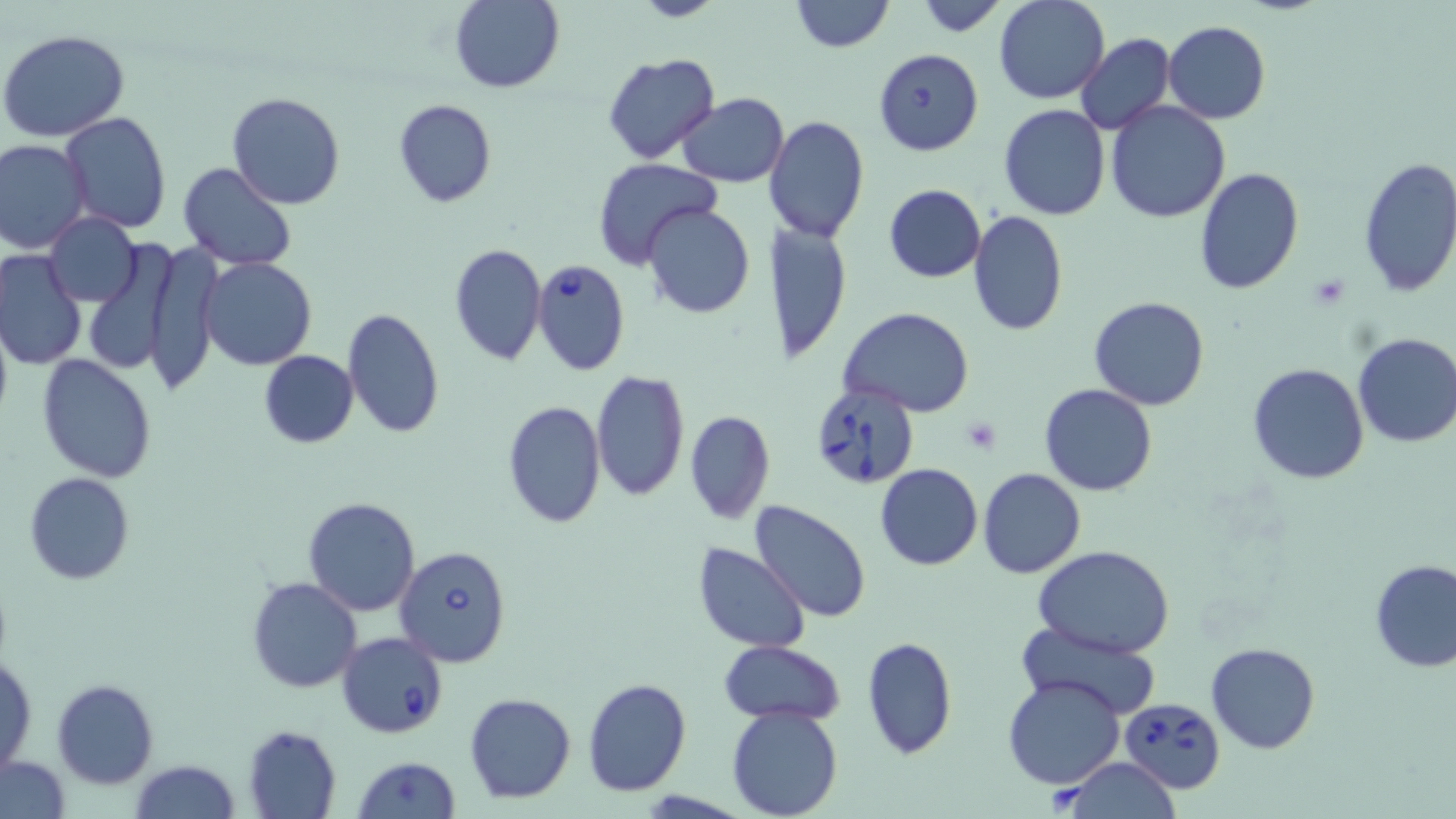
Approximate bounding boxes as (x1, y1, x2, y2) in pixels. Platelet locations: (959, 415, 1003, 453). Babesia divergens-infected red blood cell locations: (873, 48, 982, 157), (530, 258, 631, 376), (809, 380, 920, 489), (394, 543, 513, 667), (338, 632, 449, 738), (1119, 697, 1225, 795). Uninfected red blood cell locations: (449, 0, 565, 93), (790, 0, 892, 51), (913, 0, 1011, 36), (993, 0, 1109, 104), (1163, 20, 1271, 123), (1, 30, 130, 142), (1075, 34, 1174, 136), (604, 52, 719, 162), (227, 91, 345, 209), (676, 93, 789, 188), (393, 98, 496, 207), (1105, 100, 1232, 223), (999, 104, 1109, 220), (60, 111, 171, 231), (763, 115, 870, 244), (0, 139, 92, 255), (1356, 155, 1456, 298), (592, 158, 722, 272), (178, 163, 299, 271), (1193, 168, 1304, 295), (882, 184, 985, 283), (643, 203, 755, 318), (967, 210, 1069, 336), (45, 211, 142, 307), (767, 220, 851, 366), (83, 238, 181, 377), (146, 240, 223, 398), (448, 243, 546, 366), (0, 250, 87, 371), (200, 257, 316, 370), (1088, 295, 1210, 411), (341, 307, 442, 440), (839, 308, 974, 416), (0, 312, 12, 429), (1352, 331, 1456, 448), (257, 350, 360, 449), (36, 353, 158, 482), (1246, 363, 1370, 485), (590, 369, 691, 505), (1041, 383, 1157, 495), (502, 400, 605, 531), (684, 410, 774, 525), (874, 463, 984, 571), (977, 468, 1087, 580), (23, 472, 135, 584), (302, 496, 421, 617), (750, 500, 871, 622), (693, 543, 811, 653), (1035, 546, 1175, 657), (1369, 559, 1456, 672), (246, 576, 362, 692), (1014, 619, 1161, 720), (861, 636, 957, 761), (719, 640, 845, 725), (1206, 641, 1319, 754), (1, 657, 37, 771), (1003, 675, 1125, 789), (582, 677, 692, 796), (52, 678, 158, 788), (463, 691, 577, 805), (726, 704, 845, 819), (243, 724, 342, 818), (2, 755, 70, 818), (353, 757, 461, 818), (1060, 758, 1183, 818), (129, 760, 241, 819). Slide-level diagnosis: Babesia divergens. One field of a larger specimen. Light microscopy. May-Grünwald-Giemsa stain. Thin blood smear. Image is 1456×819 pixels. 1000x magnification.